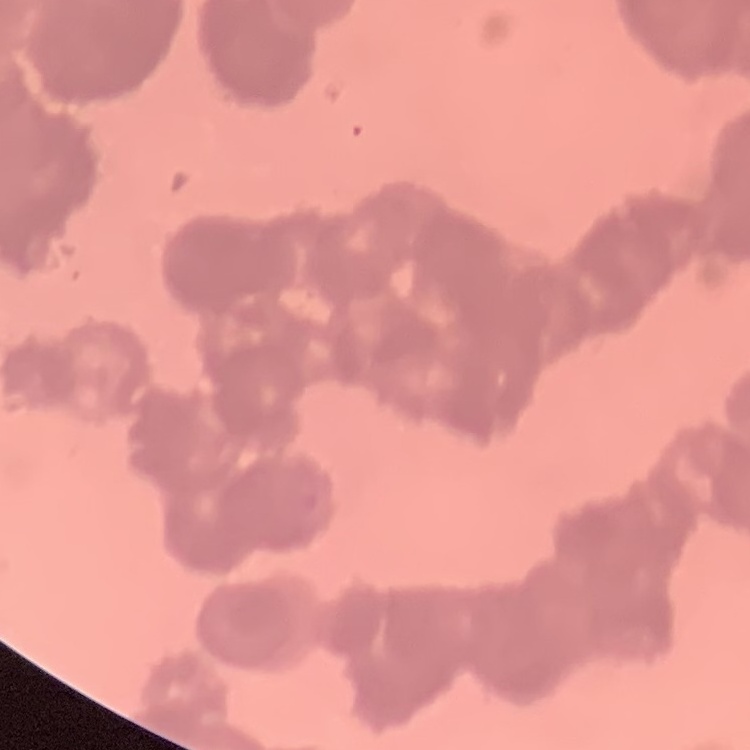

The erythrocytes exhibit rouleaux formation. One tile cut from a larger photomicrograph. Thin blood smear. Field's or Giemsa stain.